Classify this cell by malaria status.
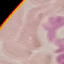

It is uninfected.

Summary:
  - Image type: cell patch, automatically extracted from a larger field of view and resized to 64 × 64 pixels
  - Preparation: thin blood smear
  - Stain: Giemsa
  - Capture: smartphone through the microscope eyepiece